Outline each Plasmodium ovale-infected red blood cell.
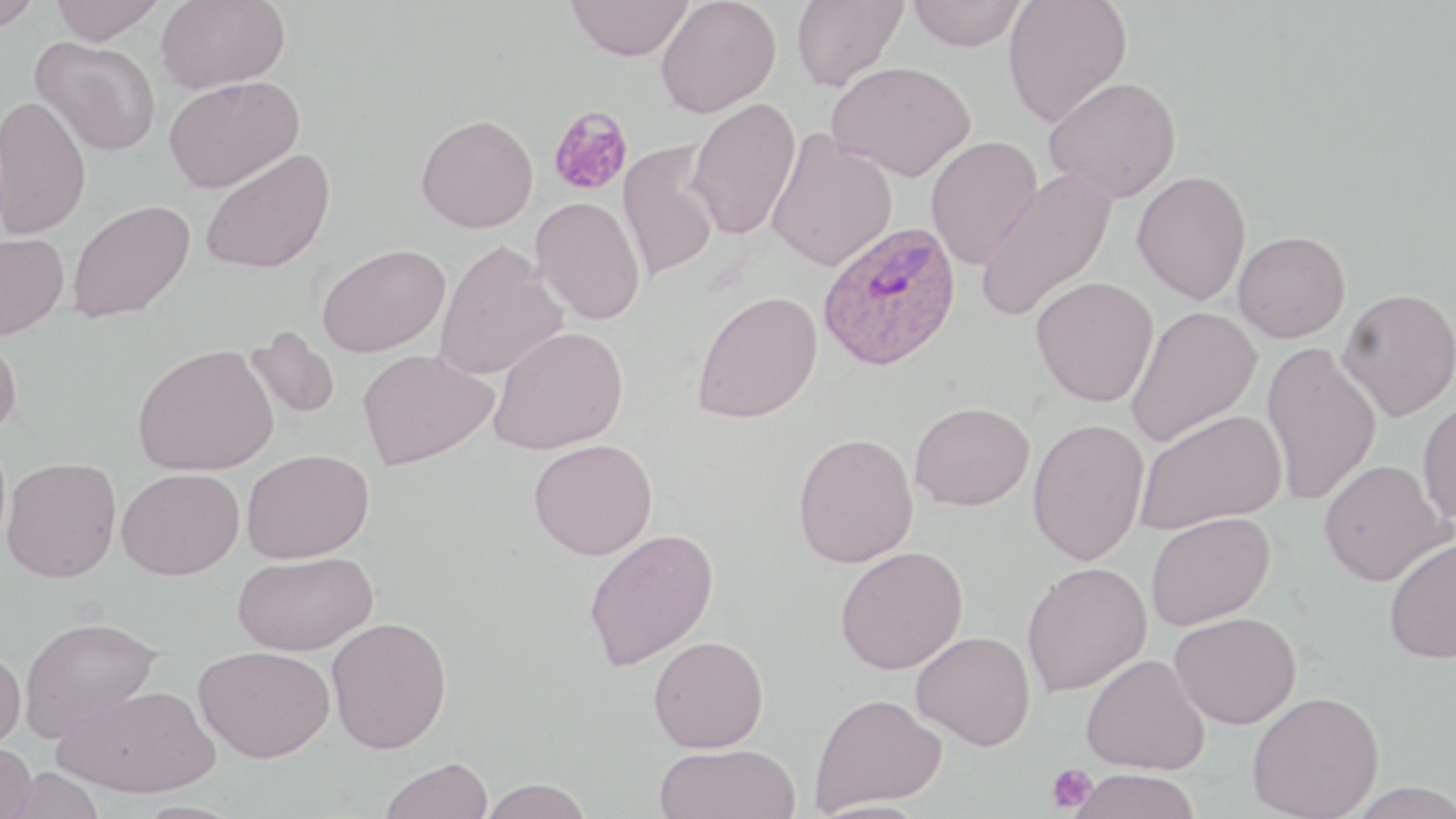
Approximate bounding boxes as (x1,y1)-(x2,y2) corner pairs in pixels.
Plasmodium ovale-infected red blood cells: (817,221)-(962,372).

Summary:
  - Platelet locations: (1044,763)-(1097,815)
  - Uninfected red blood cell locations: (0,0)-(46,32), (49,0)-(166,43), (156,0)-(290,93), (566,0)-(693,61), (655,0)-(781,118), (791,0)-(908,91), (906,0)-(1027,51), (1002,0)-(1132,128), (31,36)-(162,157), (827,61)-(976,182), (164,76)-(304,193), (1044,76)-(1182,203), (0,94)-(91,240), (687,97)-(802,239), (547,106)-(634,196), (416,113)-(539,232), (765,129)-(898,272), (925,135)-(1043,270), (617,141)-(720,283), (200,148)-(335,274), (975,170)-(1117,322), (1132,170)-(1251,305), (531,197)-(646,325), (68,199)-(195,323), (1233,231)-(1350,343), (0,232)-(69,340), (433,241)-(568,380), (316,243)-(450,357), (1031,276)-(1160,407), (1338,287)-(1456,421), (692,290)-(823,424), (1126,306)-(1262,446), (246,326)-(341,419), (488,326)-(628,455), (0,330)-(23,438), (1260,342)-(1381,506), (133,343)-(279,476), (356,349)-(498,471), (1417,399)-(1456,527), (909,400)-(1035,511), (1135,409)-(1286,534), (1027,417)-(1149,566), (792,432)-(919,568), (528,438)-(658,560), (242,448)-(374,563), (1,456)-(122,583), (1318,459)-(1451,586), (116,467)-(244,580), (1146,511)-(1275,631), (583,528)-(719,671), (1384,535)-(1456,663), (835,546)-(968,674), (232,551)-(378,655), (1021,562)-(1152,697), (1169,612)-(1301,729), (18,615)-(162,742), (326,616)-(452,753), (911,630)-(1036,751), (648,635)-(769,752), (194,644)-(335,763), (0,647)-(26,753), (1081,653)-(1211,775), (52,683)-(220,798), (1247,691)-(1384,819), (810,693)-(946,813), (0,742)-(37,819), (654,743)-(802,819), (380,757)-(494,819), (4,766)-(106,819), (1067,768)-(1201,819), (478,778)-(593,818), (1343,781)-(1456,819), (805,799)-(937,819)
  - Slide-level diagnosis: Plasmodium ovale
  - Image size: 1456×819 pixels
  - Magnification: 1000x
  - Field of view: single
  - Stain: May-Grünwald-Giemsa
  - Preparation: thin blood film
  - Modality: optical microscopy